Look for Plasmodium parasites.
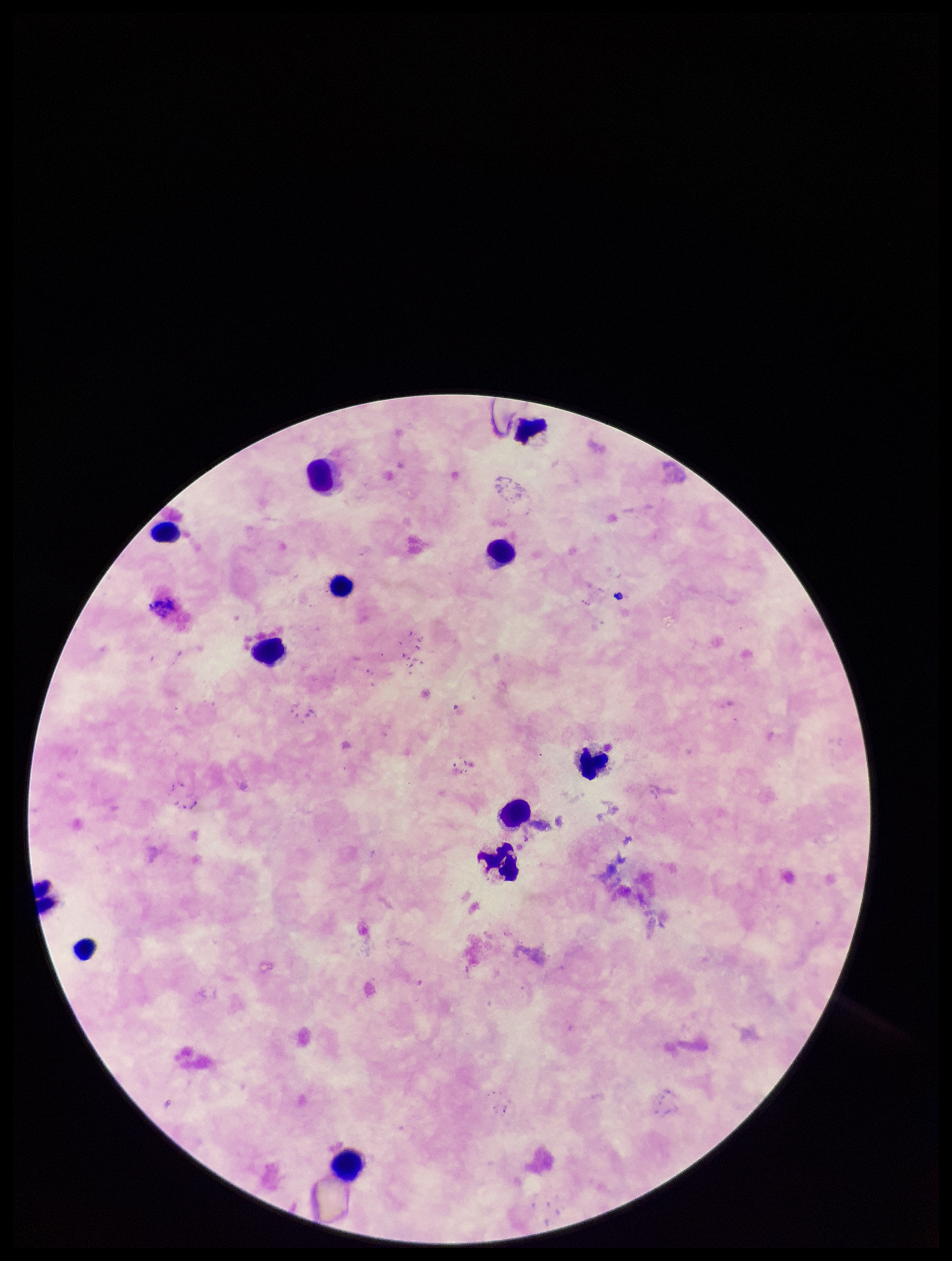
None seen.

species reported for this patient = Plasmodium falciparum
patient malaria status = positive
parasite count = 0
capture = smartphone photograph through the microscope eyepiece
image size = 952×1261 pixels
stain = Giemsa
field of view = single
leukocyte count = 12
preparation = thick